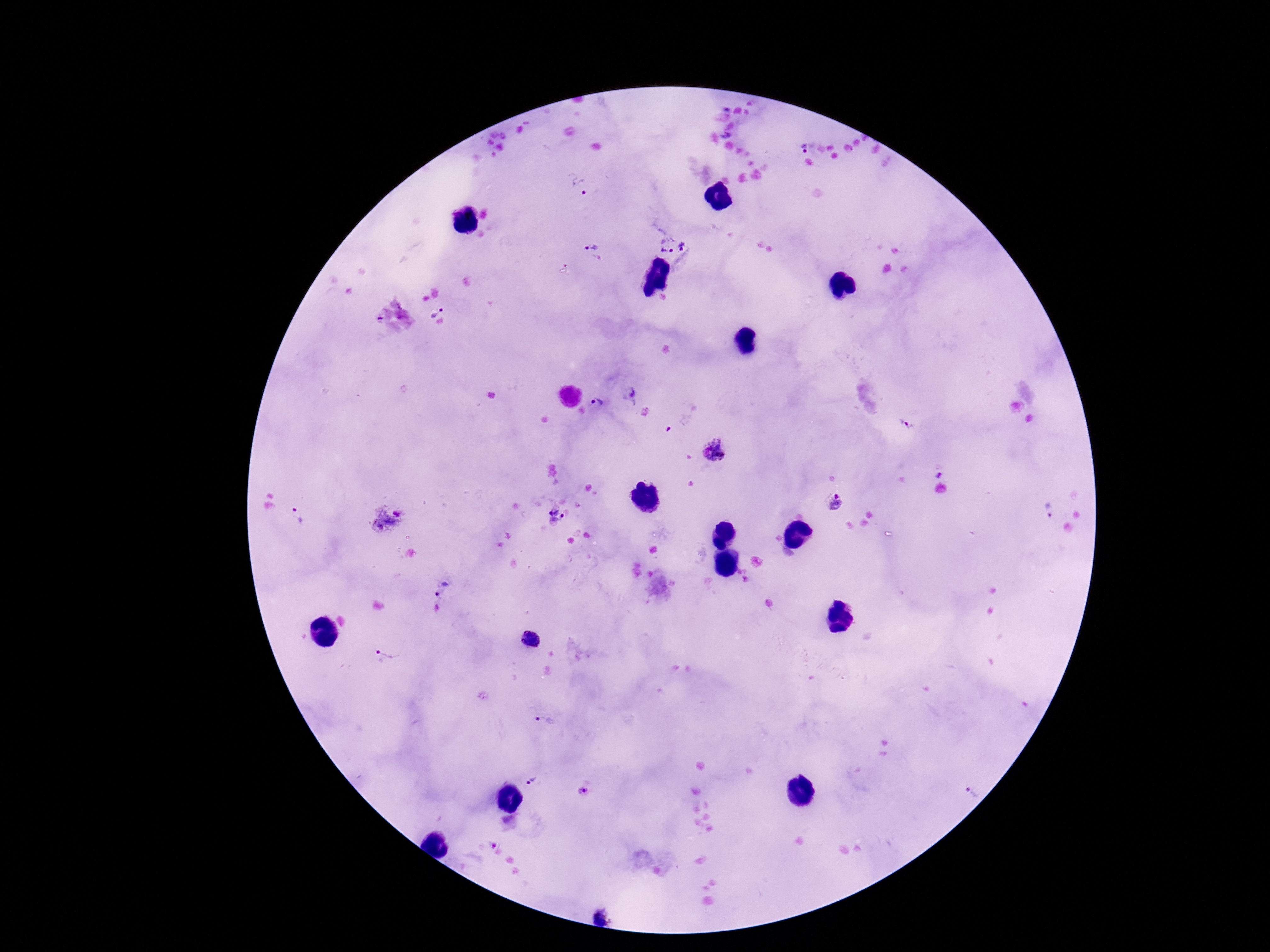

Approximate centers as [x, y] in pixels.
Summary:
  - Plasmodium parasite locations: [726, 135], [802, 146], [578, 187], [685, 246], [590, 247], [667, 248], [435, 309], [379, 318], [630, 393], [598, 403], [905, 425], [715, 451], [938, 475], [834, 503], [1049, 510], [297, 516], [554, 516], [386, 520], [442, 588], [531, 638], [384, 658], [543, 720], [530, 780], [970, 791], [584, 793], [601, 918]
  - Image size: 1270×952 pixels
  - Stain: Giemsa
  - Field of view: single
  - Preparation: thick blood film
  - Capture: smartphone camera through the microscope eyepiece
  - Patient malaria status: positive
  - Magnification: 100x